Classify this cell by malaria status.
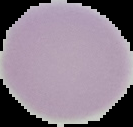
Uninfected.

Image is 133×127 pixels. Segmented cell region on a black background. From a thin blood film.